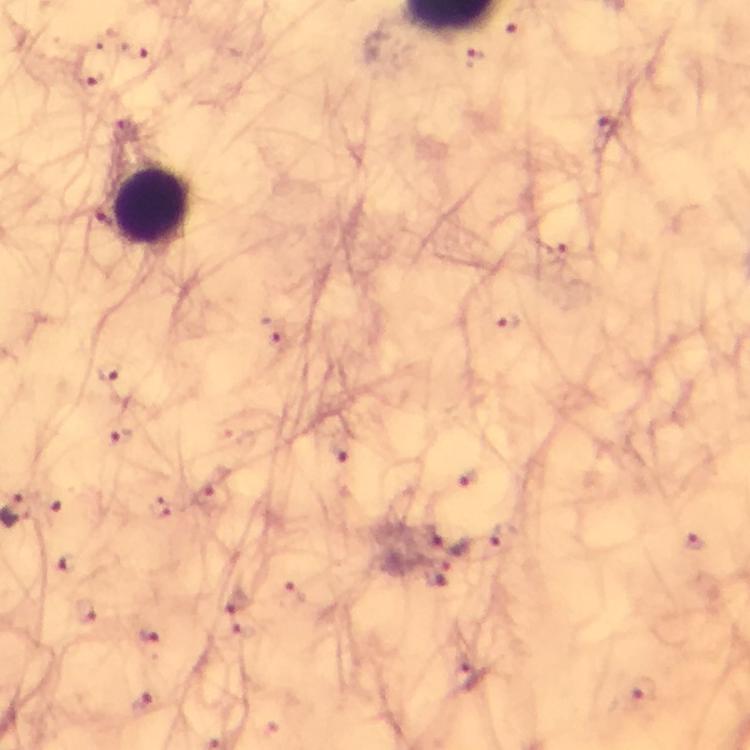
capture = smartphone mounted on the microscope
preparation = thick smear
Plasmodium parasite locations = approximate centers as {x, y} in pixels: {134, 49}, {473, 58}, {90, 79}, {606, 127}, {556, 249}, {505, 322}, {271, 332}, {109, 372}, {121, 439}, {344, 450}, {470, 480}, {213, 497}, {55, 514}, {502, 537}, {694, 543}, {72, 566}, {439, 572}, {297, 593}, {239, 601}, {86, 610}, {147, 635}, {467, 674}, {642, 689}, {143, 704}
immersion oil = applied
leukocyte locations = approximate centers as {x, y} in pixels: {154, 208}
magnification = 100x
stain = Giemsa
context = from a malaria diagnostic workup
cropped from = one field of view
image size = 750×750 pixels